Outline each uninfected red blood cell.
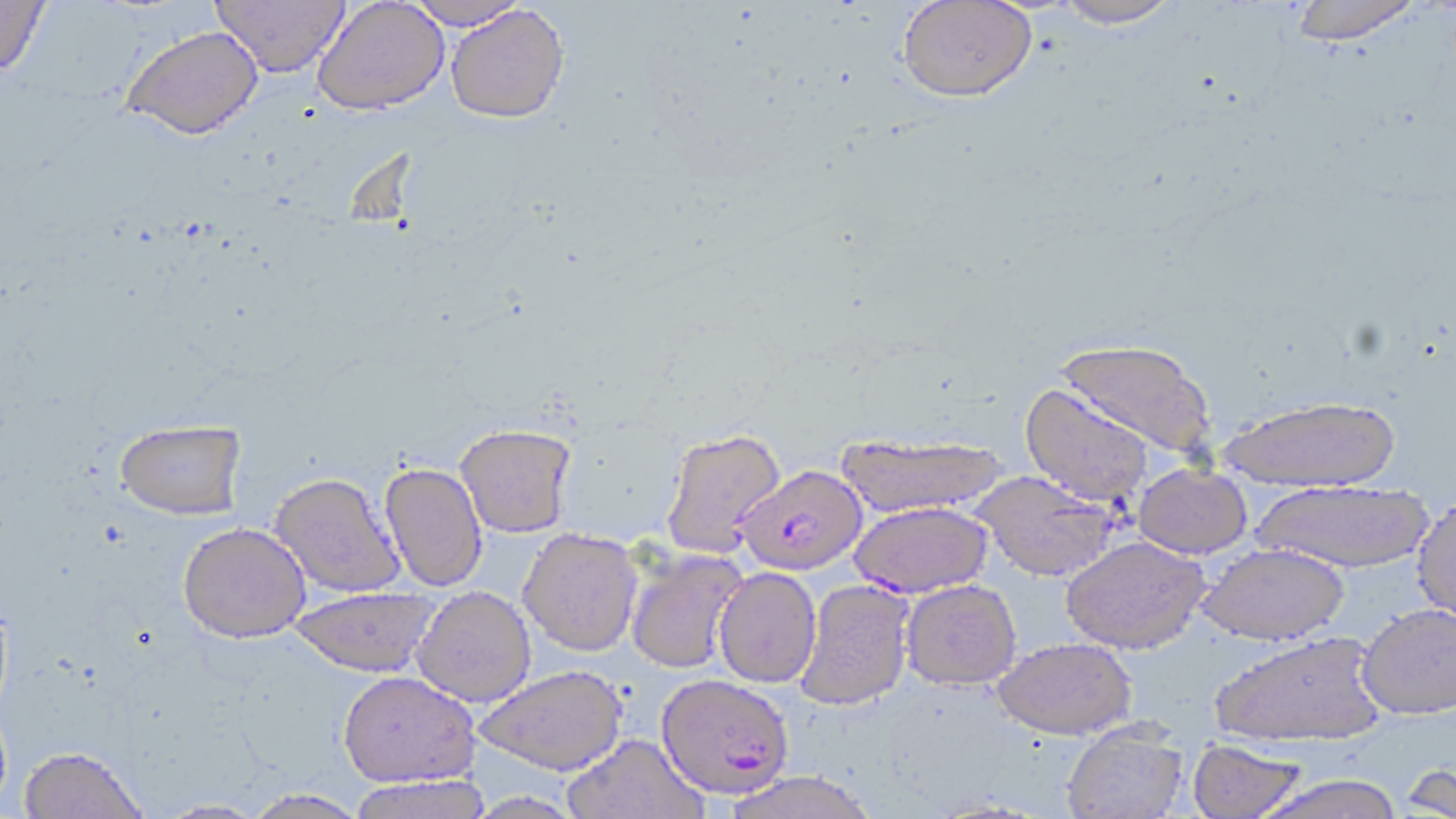
Approximate bounding boxes as [x1, y1, x2, y2] in pixels.
Uninfected red blood cells: [0, 0, 51, 81], [211, 0, 350, 78], [404, 0, 530, 30], [897, 0, 1038, 102], [1054, 0, 1181, 28], [1288, 0, 1422, 44], [312, 1, 449, 115], [445, 5, 570, 124], [122, 26, 264, 141], [1055, 337, 1217, 458], [1020, 384, 1154, 506], [1222, 394, 1402, 492], [114, 417, 248, 521], [455, 423, 576, 538], [660, 426, 787, 558], [835, 431, 1007, 518], [380, 462, 488, 592], [1133, 463, 1252, 558], [975, 470, 1119, 580], [268, 472, 404, 597], [1255, 479, 1433, 572], [1412, 496, 1456, 626], [178, 523, 310, 643], [518, 528, 642, 656], [1061, 536, 1209, 653], [1199, 543, 1348, 645], [626, 551, 748, 674], [714, 567, 821, 687], [901, 579, 1022, 689], [794, 580, 914, 711], [412, 586, 536, 706], [292, 587, 439, 676], [1357, 603, 1456, 719], [1210, 631, 1386, 748], [992, 637, 1137, 739], [475, 665, 628, 775], [338, 671, 480, 787], [0, 700, 13, 816], [1062, 722, 1190, 819], [563, 734, 707, 819], [1187, 739, 1307, 818], [17, 746, 145, 819], [720, 771, 879, 819], [1254, 774, 1405, 819], [347, 775, 493, 819], [241, 788, 370, 818], [153, 800, 271, 818].

Summary:
  - Plasmodium falciparum-infected red blood cell locations: [736, 466, 867, 575], [850, 501, 993, 597], [655, 673, 795, 799]
  - Slide-level diagnosis: Plasmodium falciparum
  - Field of view: one of a larger specimen
  - Magnification: 1000x
  - Stain: May-Grünwald-Giemsa
  - Preparation: thin blood smear
  - Image size: 1456×819 pixels
  - Modality: light microscopy